Identify the cell.
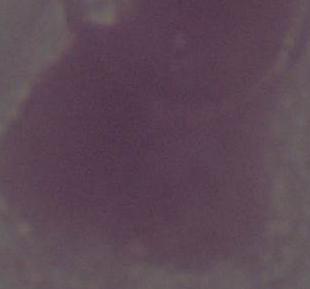

This is an erythrocyte.

Captured at 1000x magnification. Photomicrograph.